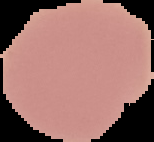

malaria status = uninfected
image type = segmented cell region with the area outside set to black
image size = 154×142 pixels
preparation = thin blood smear